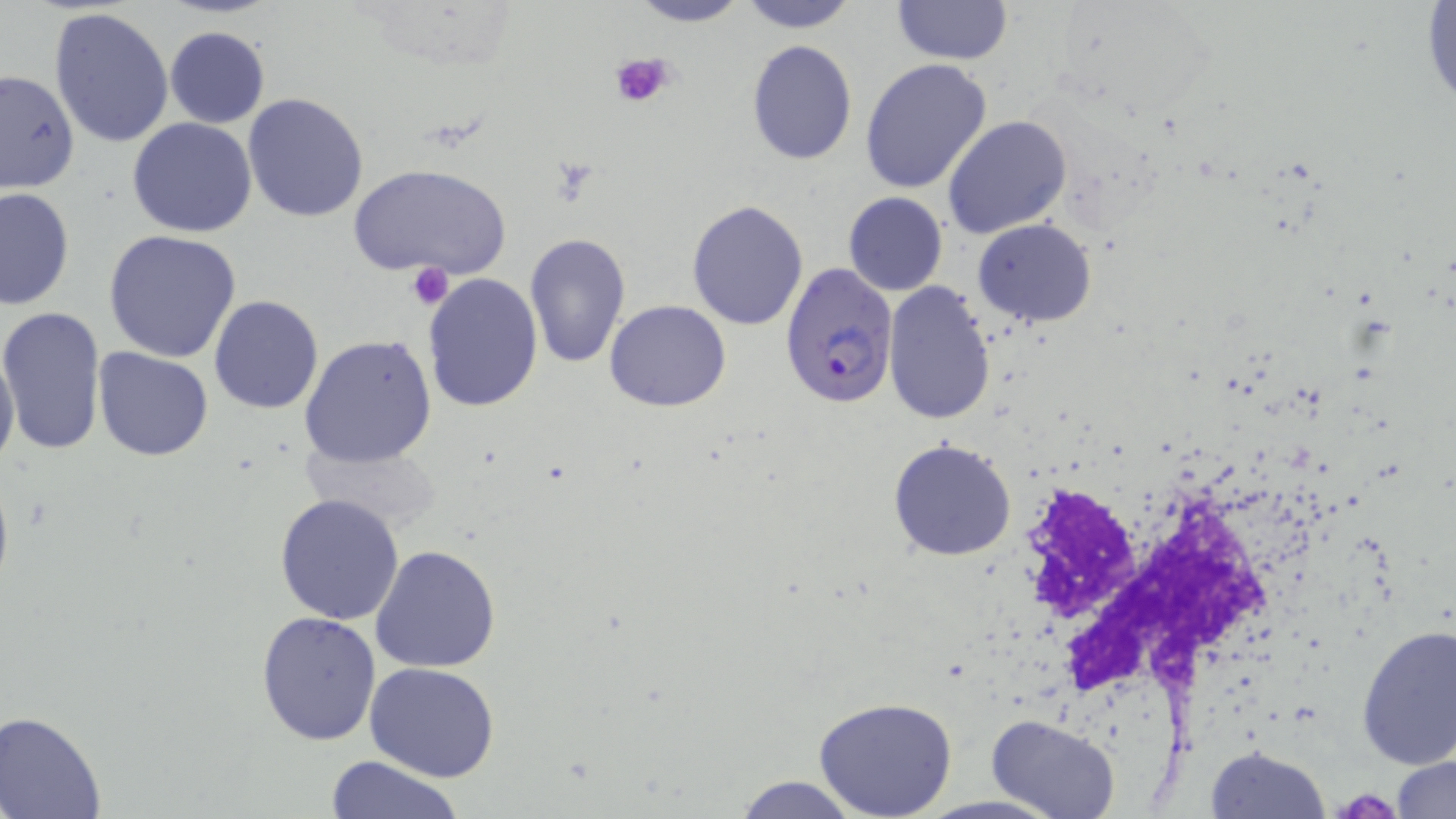

Summary:
  - Coordinate format: approximate bounding boxes as (x1, y1, x2, y2) in pixels
  - Uninfected red blood cell locations: (625, 0, 753, 27), (737, 0, 859, 32), (889, 0, 1013, 66), (1421, 2, 1456, 113), (48, 6, 177, 148), (164, 26, 270, 129), (746, 39, 858, 165), (860, 57, 993, 195), (0, 69, 78, 194), (242, 93, 370, 223), (944, 116, 1072, 239), (127, 118, 258, 238), (351, 163, 511, 282), (1, 187, 74, 311), (842, 192, 948, 296), (686, 200, 808, 330), (973, 218, 1095, 327), (101, 228, 243, 363), (524, 233, 631, 371), (421, 273, 543, 412), (884, 283, 995, 424), (208, 295, 323, 413), (605, 300, 731, 412), (0, 306, 106, 455), (299, 335, 439, 469), (0, 338, 20, 479), (93, 346, 214, 460), (888, 437, 1018, 561), (302, 439, 443, 530), (275, 494, 405, 625), (369, 545, 501, 673), (255, 610, 383, 744), (1356, 624, 1456, 769), (364, 662, 500, 783), (812, 697, 958, 818), (1, 712, 108, 819), (986, 715, 1121, 819), (1206, 745, 1328, 818), (1390, 753, 1456, 819), (324, 755, 467, 818), (733, 775, 864, 819)
  - Plasmodium falciparum-infected red blood cell locations: (780, 264, 897, 409)
  - Platelet locations: (611, 51, 677, 110), (404, 263, 455, 310), (1337, 789, 1398, 818)
  - White blood cell locations: (1022, 466, 1305, 735)
  - Slide-level diagnosis: Plasmodium falciparum
  - Preparation: thin blood film
  - Modality: optical microscopy
  - Stain: May-Grünwald-Giemsa
  - Field of view: single
  - Image size: 1456×819 pixels
  - Magnification: 1000x